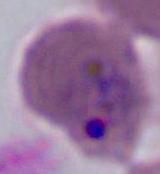

modality = photomicrograph
identification = Plasmodium
magnification = 400x or 1000x